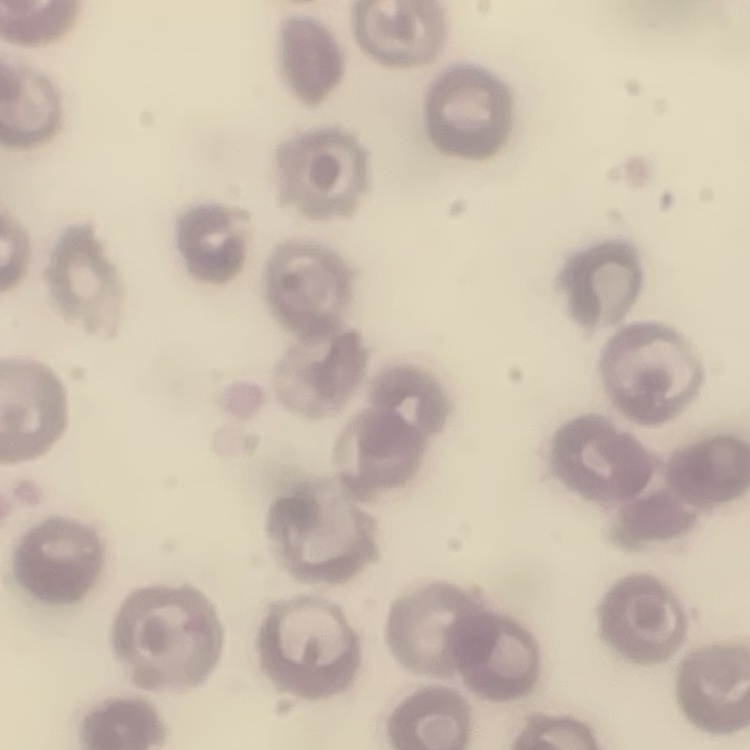

The erythrocytes exhibit no rouleaux formation. Stained with either Field's or Giemsa. Thin peripheral smear. One tile cut from a larger photomicrograph.